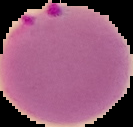
preparation = thin blood film
result = Plasmodium parasites detected
image size = 133×127 pixels
image type = cell region segmented out of the field of view; surrounding area masked to black